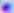

identification = Toxoplasma gondii
modality = photomicrograph
magnification = 400x